Evaluate for Plasmodium parasites.
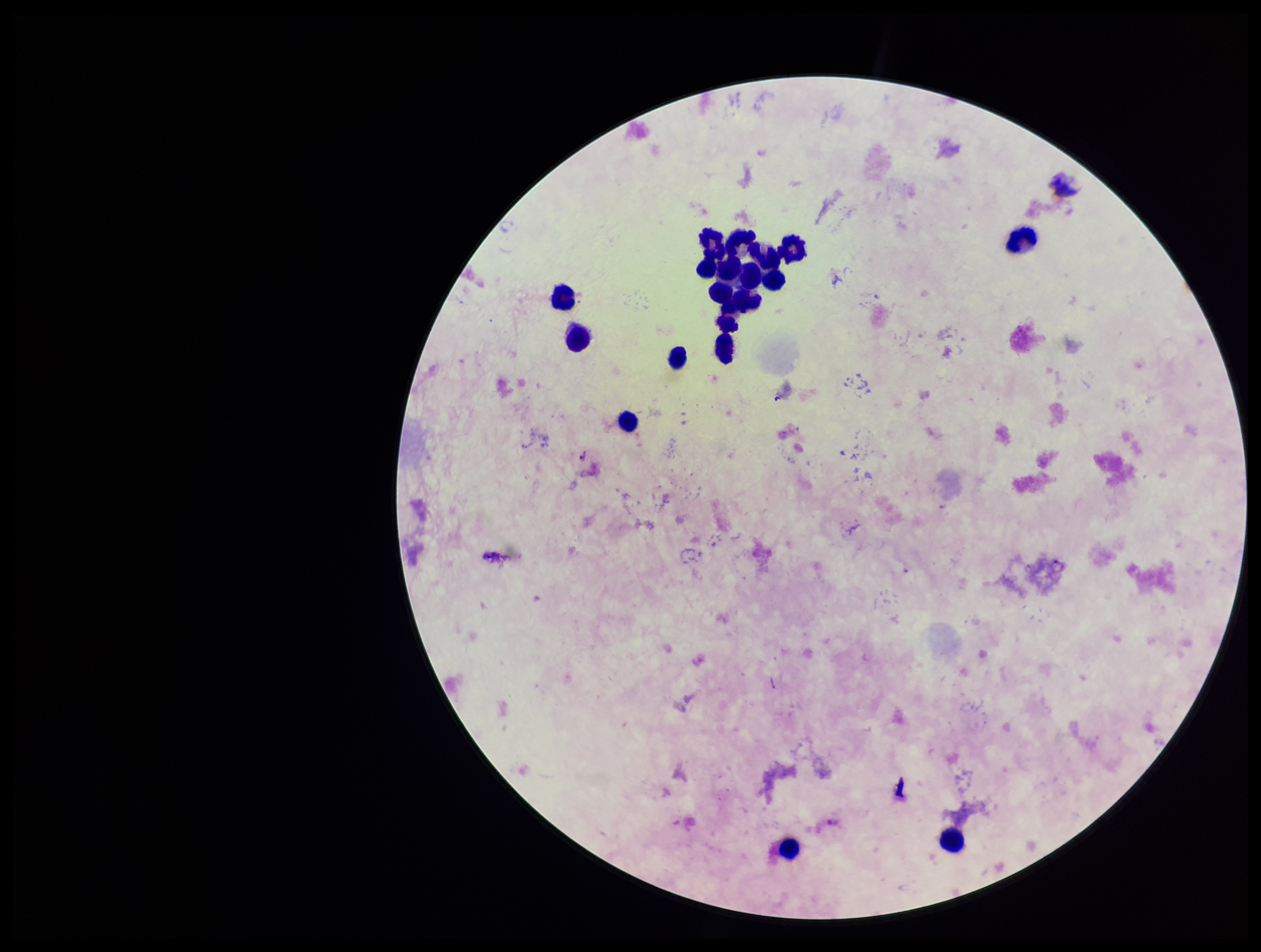
Detected.

Giemsa stain. Smartphone photograph taken through the eyepiece of a microscope. Leukocyte count: 19. Parasite count: 2. Patient malaria status: positive. Preparation: thick blood smear. Single field of view. Image is 1261×952 pixels. Species reported for this patient: Plasmodium vivax.